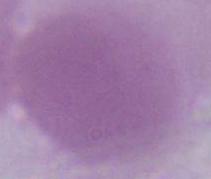

Summary:
  - Modality: photomicrograph
  - Identification: red blood cell
  - Magnification: 1000x